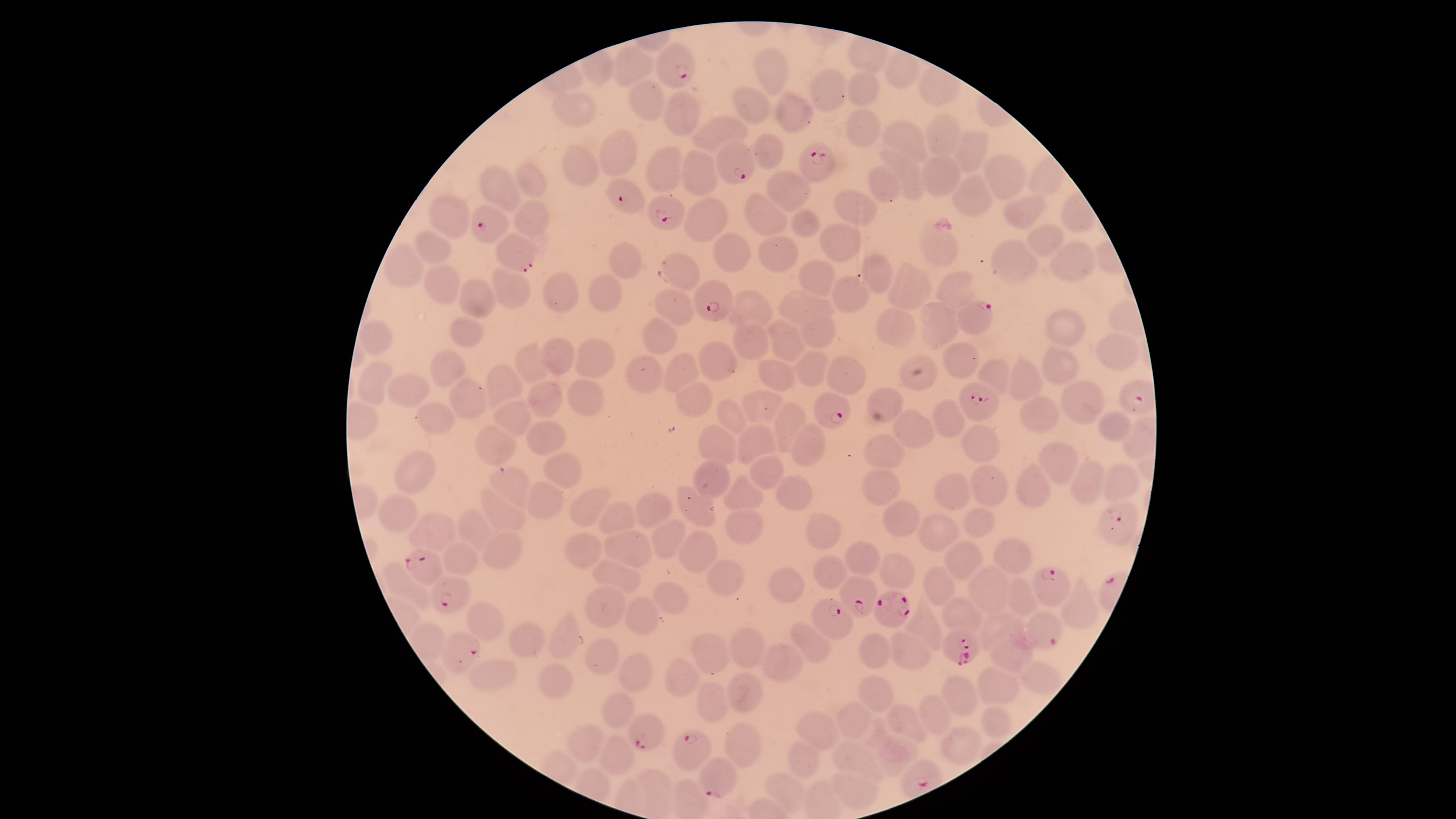
Approximate marker points as (x, y) in pixels. Parasitized red blood cells: (677, 55), (740, 153), (815, 168), (630, 189), (672, 204), (494, 216), (517, 250), (716, 290), (972, 317), (830, 402), (979, 405), (511, 483), (1113, 533), (432, 568), (456, 589), (860, 589), (1058, 591), (892, 614), (835, 618), (1041, 621), (456, 642), (951, 645), (651, 722), (695, 751), (722, 773). Uninfected red blood cells: (775, 69), (632, 73), (899, 73), (866, 88), (835, 92), (752, 103), (651, 105), (794, 108), (575, 111), (676, 111), (856, 129), (719, 130), (903, 136), (943, 136), (967, 148), (619, 154), (766, 154), (693, 168), (585, 170), (670, 172), (911, 172), (997, 172), (939, 177), (532, 179), (496, 180), (786, 185), (886, 187), (966, 197), (853, 210), (1017, 211), (703, 215), (768, 215), (803, 218), (448, 219), (534, 226), (1041, 232), (837, 234), (946, 245), (732, 248), (433, 249), (777, 250), (623, 258), (1014, 259), (1068, 260), (678, 262), (399, 268), (870, 271), (816, 277), (903, 281), (437, 283), (947, 285), (507, 286), (605, 292), (564, 293), (841, 295), (802, 302), (475, 303), (679, 308), (749, 308), (1066, 322), (899, 323), (938, 326), (817, 329), (468, 331), (372, 332), (663, 339), (749, 339), (784, 345), (1121, 347), (563, 356), (594, 357), (965, 358), (716, 364), (535, 365), (1061, 367), (447, 369), (676, 370), (814, 372), (851, 374), (921, 375), (997, 375), (646, 378), (773, 379), (508, 380), (1031, 380), (379, 385), (414, 390), (885, 396), (467, 397), (585, 397), (690, 397), (1083, 399), (552, 401), (762, 404), (512, 413), (944, 413), (1044, 413), (732, 416), (436, 419), (790, 421), (910, 425), (1111, 425), (545, 434), (496, 440), (983, 442), (722, 445), (757, 446), (809, 448), (887, 449), (1060, 461), (412, 469), (561, 469), (771, 473), (710, 474), (1086, 480), (1119, 483), (991, 487), (876, 488), (1036, 489), (953, 490), (737, 494), (795, 495), (546, 504), (594, 504), (653, 505), (694, 505), (397, 512), (506, 514), (626, 517), (903, 518), (978, 522), (744, 524), (429, 529), (479, 531), (825, 531), (938, 533), (664, 536), (506, 546), (632, 548), (699, 548), (586, 550), (1007, 551), (456, 554), (963, 557), (867, 561), (611, 570), (898, 570), (828, 572), (720, 577), (943, 583), (403, 584), (786, 586), (981, 586), (1015, 591), (666, 598), (1077, 607), (608, 608), (965, 614), (482, 617), (640, 619), (925, 623), (999, 625), (520, 638), (563, 640), (815, 642), (908, 646), (745, 647), (1010, 651), (872, 652), (710, 653), (603, 662), (775, 664), (681, 673), (495, 674), (634, 676), (1037, 678), (553, 683), (994, 687), (746, 691), (875, 692), (960, 697), (712, 700), (613, 709), (938, 713), (850, 716), (904, 720), (994, 723), (821, 732), (583, 742), (960, 745), (747, 747), (897, 754), (619, 755), (855, 760), (801, 762), (778, 787), (847, 788). Presence: malaria parasites identified. Circular visible region. Thin smear of blood. Giemsa-stained preparation. Smartphone photograph through the microscope eyepiece. One field of view of the specimen. Image is 1456×819 pixels. Species: Plasmodium falciparum.